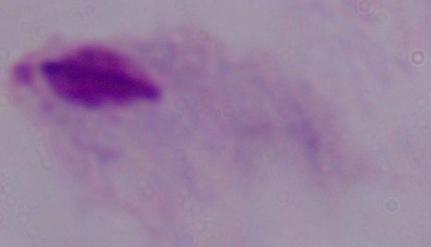
Summary:
  - Identification: trichomonad
  - Modality: micrograph
  - Magnification: 1000x